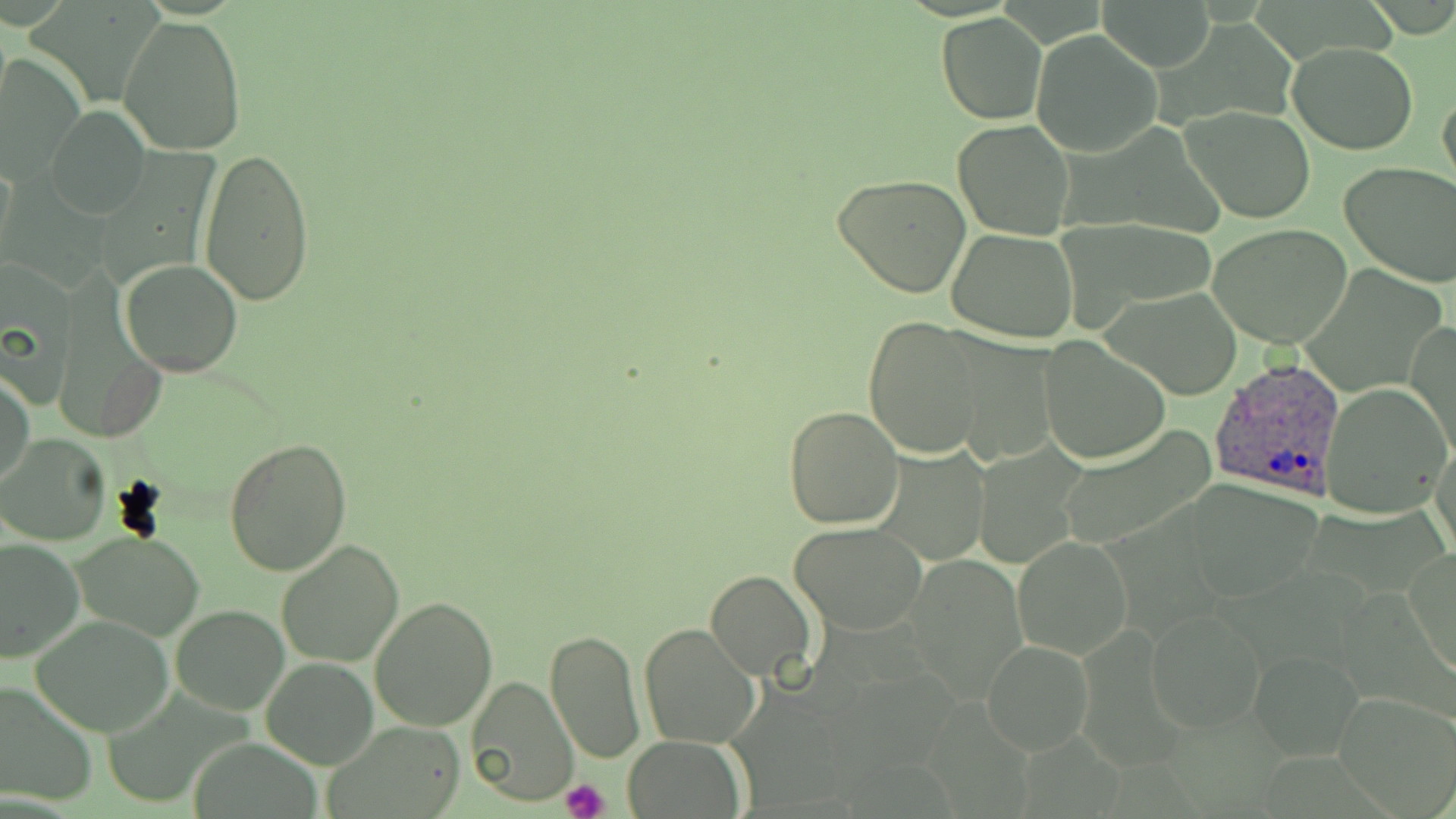 Approximate bounding boxes as named x1/y1/x2/y2 corners in pixels. Plasmodium ovale-infected red blood cell locations: (x1=1208, y1=357, x2=1350, y2=504). Platelet locations: (x1=561, y1=779, x2=610, y2=819). Uninfected red blood cell locations: (x1=1096, y1=0, x2=1214, y2=71), (x1=936, y1=14, x2=1048, y2=124), (x1=119, y1=16, x2=246, y2=156), (x1=1030, y1=30, x2=1162, y2=158), (x1=1287, y1=40, x2=1419, y2=154), (x1=1, y1=54, x2=84, y2=183), (x1=1437, y1=84, x2=1456, y2=198), (x1=1181, y1=105, x2=1316, y2=224), (x1=46, y1=108, x2=148, y2=218), (x1=953, y1=120, x2=1074, y2=240), (x1=197, y1=148, x2=315, y2=308), (x1=1339, y1=163, x2=1456, y2=286), (x1=833, y1=172, x2=971, y2=298), (x1=1052, y1=218, x2=1221, y2=325), (x1=1208, y1=223, x2=1355, y2=350), (x1=946, y1=229, x2=1079, y2=344), (x1=2, y1=257, x2=77, y2=398), (x1=119, y1=259, x2=243, y2=378), (x1=1105, y1=286, x2=1245, y2=400), (x1=863, y1=315, x2=986, y2=460), (x1=1407, y1=321, x2=1456, y2=461), (x1=950, y1=335, x2=1060, y2=466), (x1=1040, y1=335, x2=1169, y2=464), (x1=1, y1=371, x2=34, y2=489), (x1=1323, y1=385, x2=1452, y2=518), (x1=784, y1=406, x2=904, y2=529), (x1=1055, y1=425, x2=1219, y2=552), (x1=1, y1=433, x2=114, y2=547), (x1=1431, y1=433, x2=1456, y2=563), (x1=222, y1=437, x2=352, y2=578), (x1=873, y1=446, x2=991, y2=565), (x1=790, y1=522, x2=929, y2=635), (x1=72, y1=531, x2=204, y2=641), (x1=1012, y1=535, x2=1132, y2=661), (x1=1, y1=537, x2=83, y2=662), (x1=277, y1=540, x2=404, y2=667), (x1=1404, y1=547, x2=1456, y2=680), (x1=908, y1=555, x2=1027, y2=701), (x1=705, y1=571, x2=817, y2=682), (x1=368, y1=596, x2=497, y2=732), (x1=170, y1=604, x2=288, y2=714), (x1=1146, y1=607, x2=1268, y2=734), (x1=31, y1=615, x2=174, y2=737), (x1=639, y1=623, x2=761, y2=749), (x1=546, y1=629, x2=645, y2=763), (x1=983, y1=639, x2=1094, y2=755), (x1=1248, y1=651, x2=1361, y2=761), (x1=262, y1=657, x2=377, y2=768), (x1=465, y1=675, x2=578, y2=806), (x1=0, y1=683, x2=99, y2=808), (x1=1334, y1=689, x2=1456, y2=814), (x1=320, y1=720, x2=468, y2=818), (x1=621, y1=737, x2=748, y2=818). Slide-level diagnosis: Plasmodium ovale. Image is 1456×819 pixels. May-Grünwald-Giemsa-stained preparation. Light microscopy. One field of a larger specimen. 1000x magnification. Thin blood film.